Describe the morphology of the erythrocytes.
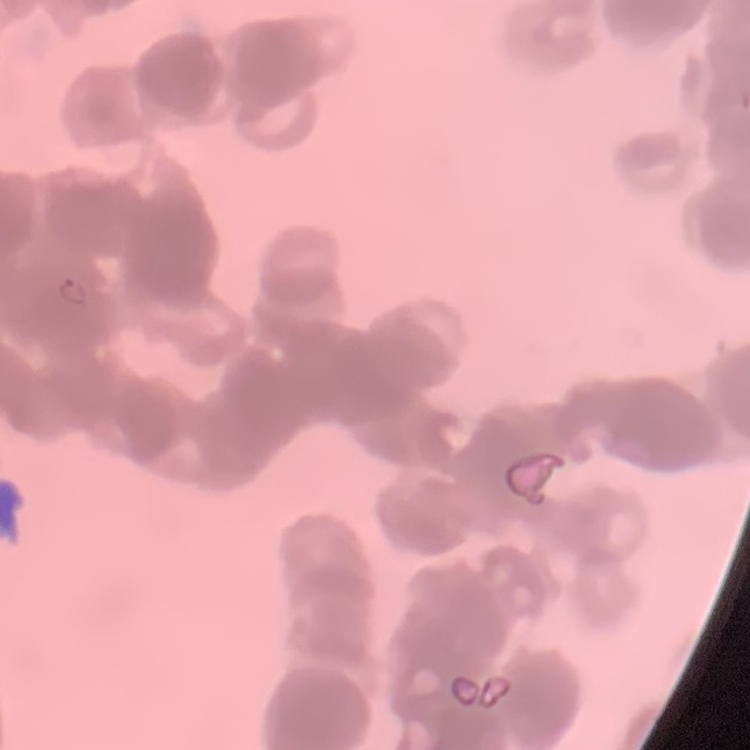
They show rouleaux formation.

Thin peripheral smear. One tile cut from a larger photomicrograph. Stained with either Field's or Giemsa.